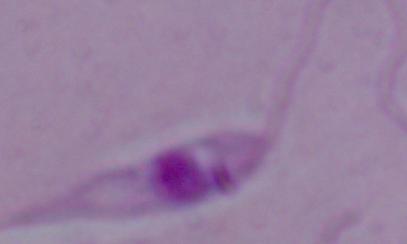
Summary:
  - Magnification: 1000x
  - Identification: Leishmania
  - Modality: micrograph